State which parasite is depicted.
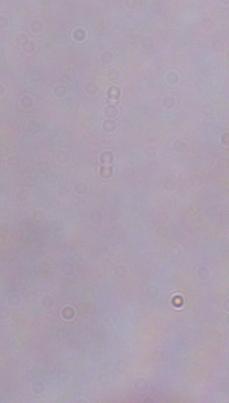

This is a trypanosome.

{
  "magnification": "1000x",
  "modality": "photomicrograph"
}